Assess this cell for malaria.
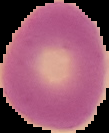

It is uninfected.

{
  "image_size": "109×133 pixels",
  "image_type": "segmented cell region with the area outside set to black",
  "preparation": "thin blood film"
}